Assess this cell for malaria.
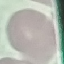

It is uninfected.

Cell patch, automatically extracted from a larger field of view and resized to 64 × 64 pixels. Photographed with a smartphone camera at the microscope eyepiece. Thin blood smear. Giemsa stain.